Locate every uninfected red blood cell.
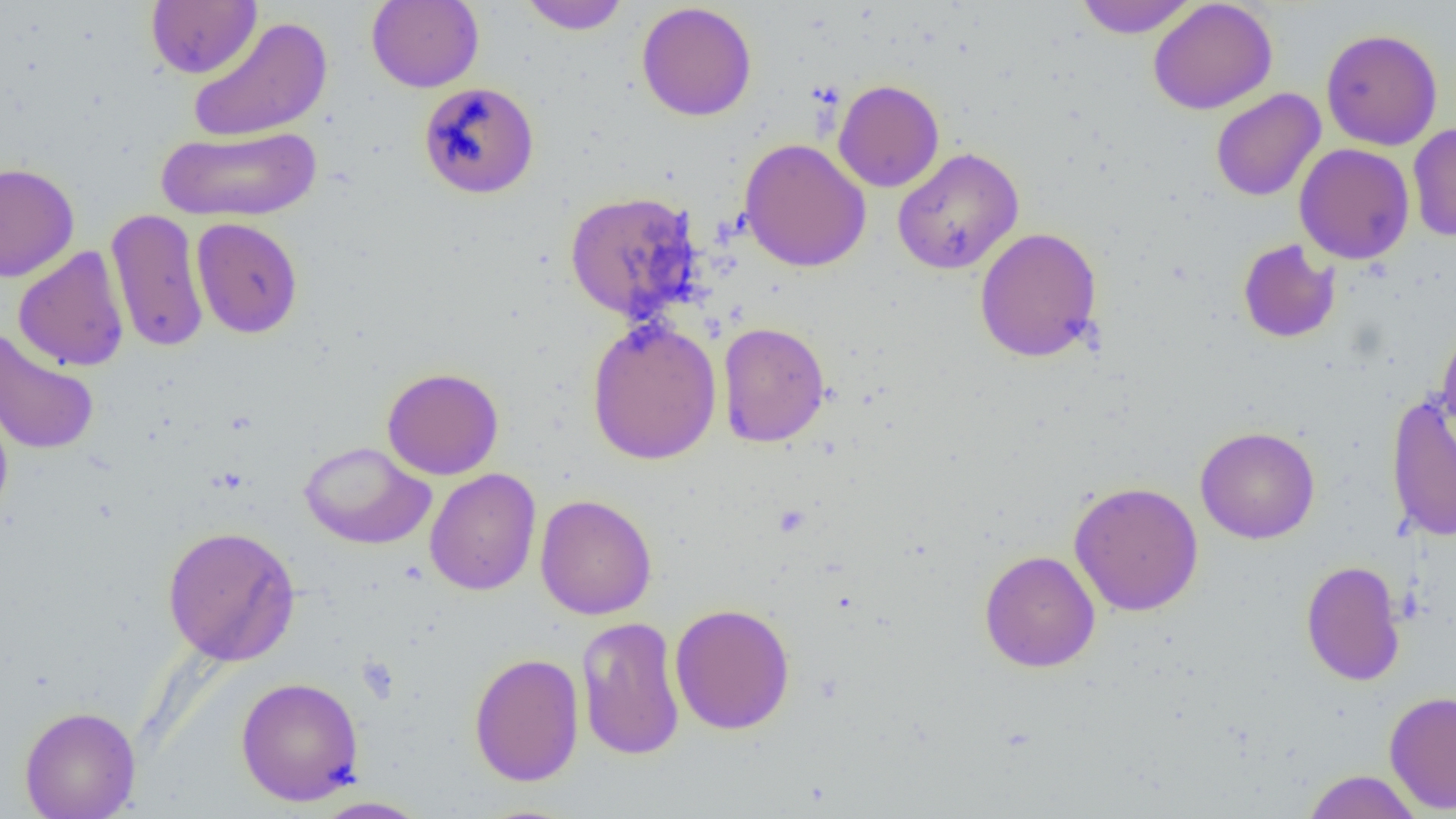
Approximate bounding boxes as (x1, y1, x2, y2) in pixels.
Uninfected red blood cells: (146, 0, 262, 79), (366, 0, 484, 92), (519, 0, 631, 34), (1074, 0, 1198, 38), (1148, 0, 1278, 115), (636, 2, 757, 122), (187, 16, 333, 143), (1321, 28, 1443, 150), (1313, 29, 1427, 263), (833, 80, 944, 192), (418, 81, 539, 199), (1210, 88, 1326, 201), (1407, 121, 1456, 242), (155, 125, 322, 222), (739, 138, 871, 272), (1294, 143, 1415, 264), (892, 147, 1024, 275), (0, 162, 80, 282), (564, 190, 702, 322), (106, 207, 209, 354), (191, 217, 303, 339), (974, 227, 1103, 363), (1237, 239, 1340, 343), (13, 245, 130, 371), (587, 318, 722, 465), (717, 321, 831, 447), (1437, 323, 1456, 444), (1, 329, 100, 456), (382, 367, 504, 480), (1385, 393, 1456, 542), (0, 400, 13, 525), (1195, 426, 1320, 544), (299, 441, 435, 550), (424, 468, 541, 595), (1069, 481, 1204, 616), (535, 494, 657, 620), (162, 525, 300, 665), (979, 550, 1101, 672), (1301, 559, 1406, 686), (669, 603, 795, 734), (576, 616, 685, 761), (468, 652, 584, 787), (236, 676, 364, 806), (1384, 690, 1456, 814), (19, 705, 141, 819), (1301, 770, 1424, 818), (309, 796, 432, 818).

slide_level_diagnosis: no evidence of blood parasites
field_of_view: single
image_size: 1456×819 pixels
magnification: 1000x
modality: light microscopy
preparation: thin blood film